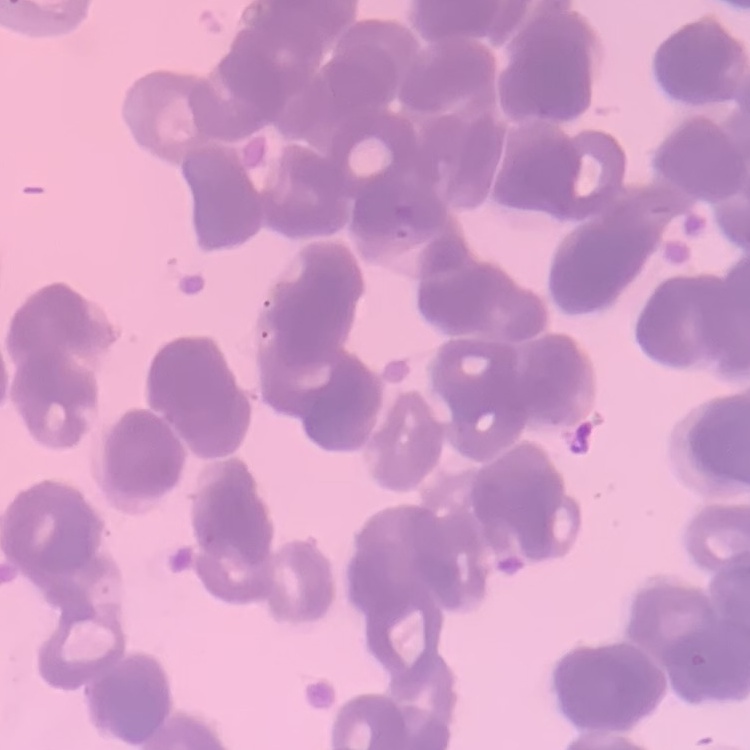
The red blood cells exhibit rouleaux formation. Stained with either Field's or Giemsa. One tile cut from a larger photomicrograph. Thin peripheral smear.